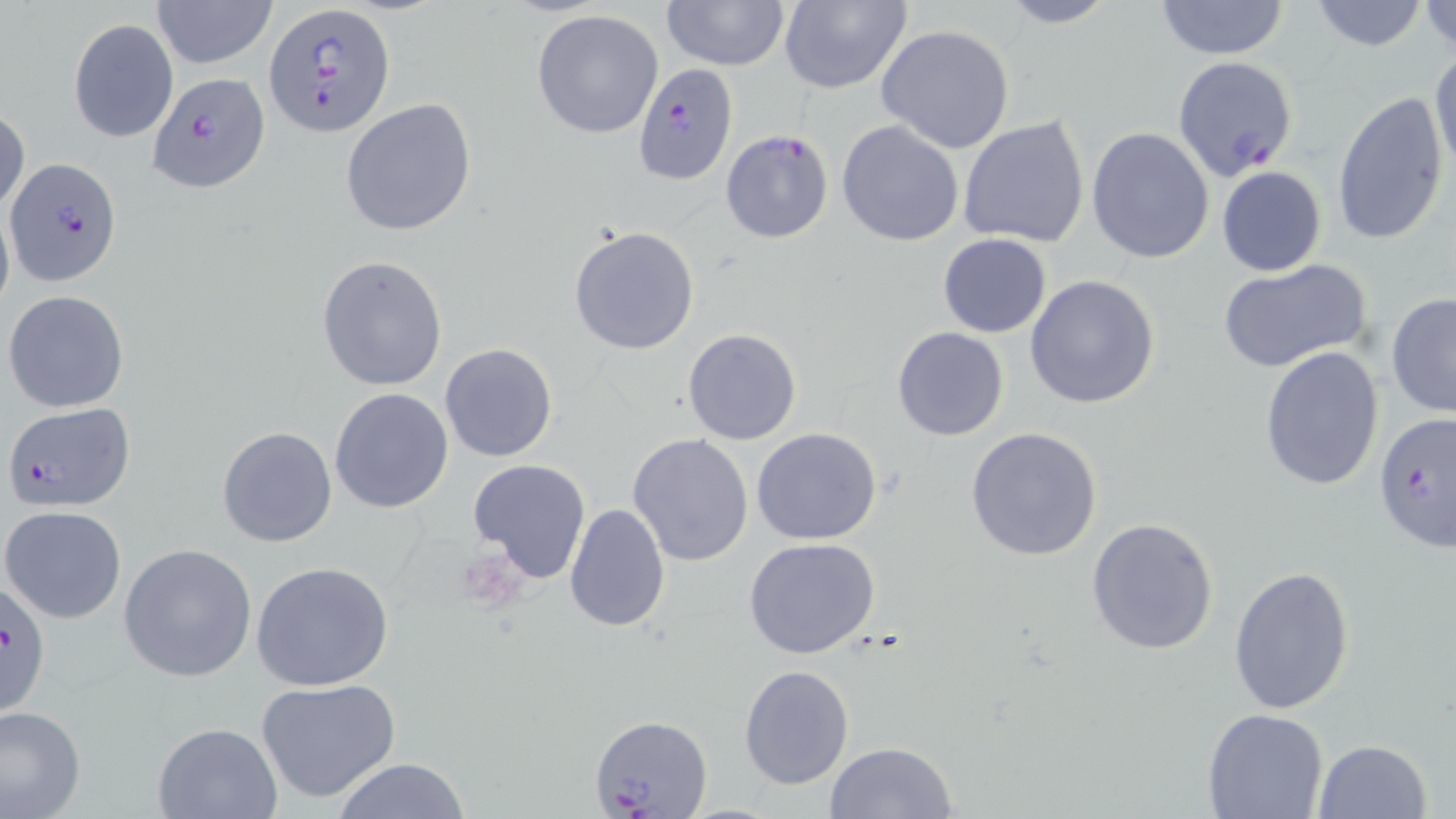

Approximate bounding boxes as (x1,y1)-(x2,y2) corner pairs in pixels. Uninfected red blood cell locations: (149,0)-(278,68), (660,0)-(789,70), (777,0)-(911,93), (995,0)-(1122,28), (1152,0)-(1292,59), (1305,0)-(1432,51), (1421,1)-(1455,57), (531,9)-(665,140), (69,18)-(178,142), (876,24)-(1018,154), (1429,48)-(1455,186), (1331,90)-(1451,246), (340,98)-(477,236), (0,107)-(28,220), (958,115)-(1090,248), (837,120)-(964,247), (1085,127)-(1216,265), (1216,167)-(1327,277), (0,198)-(14,323), (569,225)-(700,356), (938,233)-(1052,337), (317,255)-(449,393), (1216,258)-(1373,373), (1025,275)-(1160,410), (4,290)-(130,411), (1385,293)-(1456,418), (892,327)-(1008,442), (683,328)-(801,445), (439,342)-(558,462), (1259,345)-(1384,490), (330,388)-(454,514), (217,426)-(337,547), (964,426)-(1104,562), (752,427)-(884,546), (627,434)-(754,567), (467,458)-(592,583), (563,502)-(671,633), (3,505)-(128,624), (1085,517)-(1220,656), (743,537)-(882,660), (118,544)-(259,683), (250,561)-(396,691), (1229,563)-(1356,714), (737,664)-(854,790), (255,677)-(401,805), (0,704)-(85,819), (1201,709)-(1330,819), (151,722)-(282,819), (1313,737)-(1434,818), (825,742)-(957,819), (330,758)-(472,818). Plasmodium falciparum-infected red blood cell locations: (264,3)-(396,140), (1172,54)-(1299,184), (632,64)-(738,184), (150,73)-(270,194), (720,130)-(833,243), (5,156)-(121,285), (3,402)-(136,510), (1374,412)-(1456,558), (1,581)-(54,719), (589,714)-(712,817). Slide-level diagnosis: Plasmodium falciparum. Thin blood film. Image is 1456×819 pixels. May-Grünwald-Giemsa-stained preparation. Single field of view. Optical microscopy. 1000x magnification.